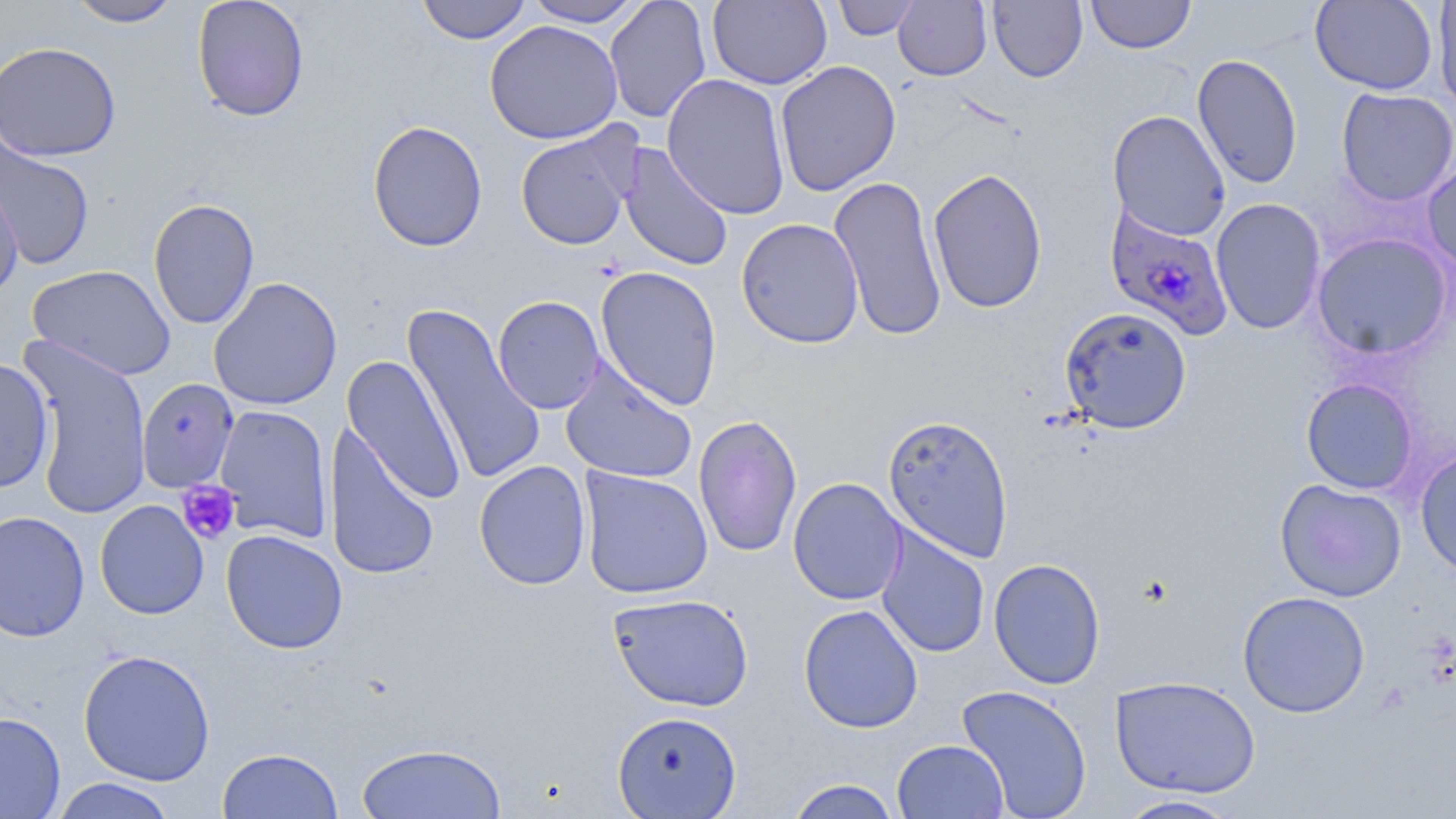

Approximate bounding boxes as [x1, y1, x2, y2] in pixels. Plasmodium falciparum-infected red blood cell locations: [1105, 204, 1235, 340]. Platelet locations: [175, 480, 240, 545]. Uninfected red blood cell locations: [66, 0, 184, 28], [191, 0, 310, 123], [416, 0, 532, 44], [523, 0, 645, 27], [605, 0, 712, 124], [707, 0, 832, 90], [832, 0, 921, 40], [893, 0, 992, 80], [988, 0, 1087, 83], [1086, 0, 1196, 54], [1433, 0, 1456, 115], [1310, 1, 1438, 95], [484, 20, 623, 144], [0, 41, 121, 161], [1191, 54, 1303, 189], [774, 60, 902, 196], [661, 73, 792, 220], [1336, 87, 1456, 207], [1107, 109, 1231, 242], [367, 119, 488, 252], [515, 125, 637, 250], [0, 132, 95, 270], [617, 142, 734, 273], [1422, 156, 1456, 277], [928, 168, 1048, 314], [0, 171, 24, 298], [828, 175, 948, 343], [147, 197, 260, 330], [1210, 198, 1327, 334], [736, 218, 865, 349], [1311, 232, 1453, 360], [27, 265, 176, 380], [595, 265, 723, 411], [208, 276, 343, 411], [493, 296, 605, 414], [402, 303, 547, 486], [1059, 306, 1193, 434], [18, 337, 152, 518], [342, 354, 467, 506], [0, 358, 54, 494], [559, 359, 697, 484], [1300, 377, 1418, 495], [136, 378, 239, 493], [213, 405, 334, 543], [693, 413, 802, 559], [882, 414, 1014, 562], [324, 424, 440, 582], [1415, 448, 1456, 578], [474, 460, 592, 591], [578, 467, 713, 599], [787, 477, 907, 606], [1274, 479, 1407, 602], [95, 499, 209, 619], [0, 510, 90, 642], [875, 525, 990, 658], [221, 529, 348, 654], [877, 537, 1103, 666], [988, 557, 1106, 690], [1237, 591, 1371, 718], [608, 592, 754, 712], [798, 604, 924, 733], [78, 649, 216, 786], [1110, 675, 1261, 798], [956, 684, 1093, 819], [612, 710, 742, 818], [0, 711, 66, 818], [891, 739, 1010, 819], [356, 741, 506, 819], [216, 747, 344, 819], [49, 778, 179, 819], [785, 778, 902, 818], [1113, 794, 1245, 818]. Slide-level diagnosis: Plasmodium falciparum. 1000x magnification. Image is 1456×819 pixels. May-Grünwald-Giemsa stain. Thin blood film. Single field of view. Light microscopy.